Point out each Plasmodium parasite.
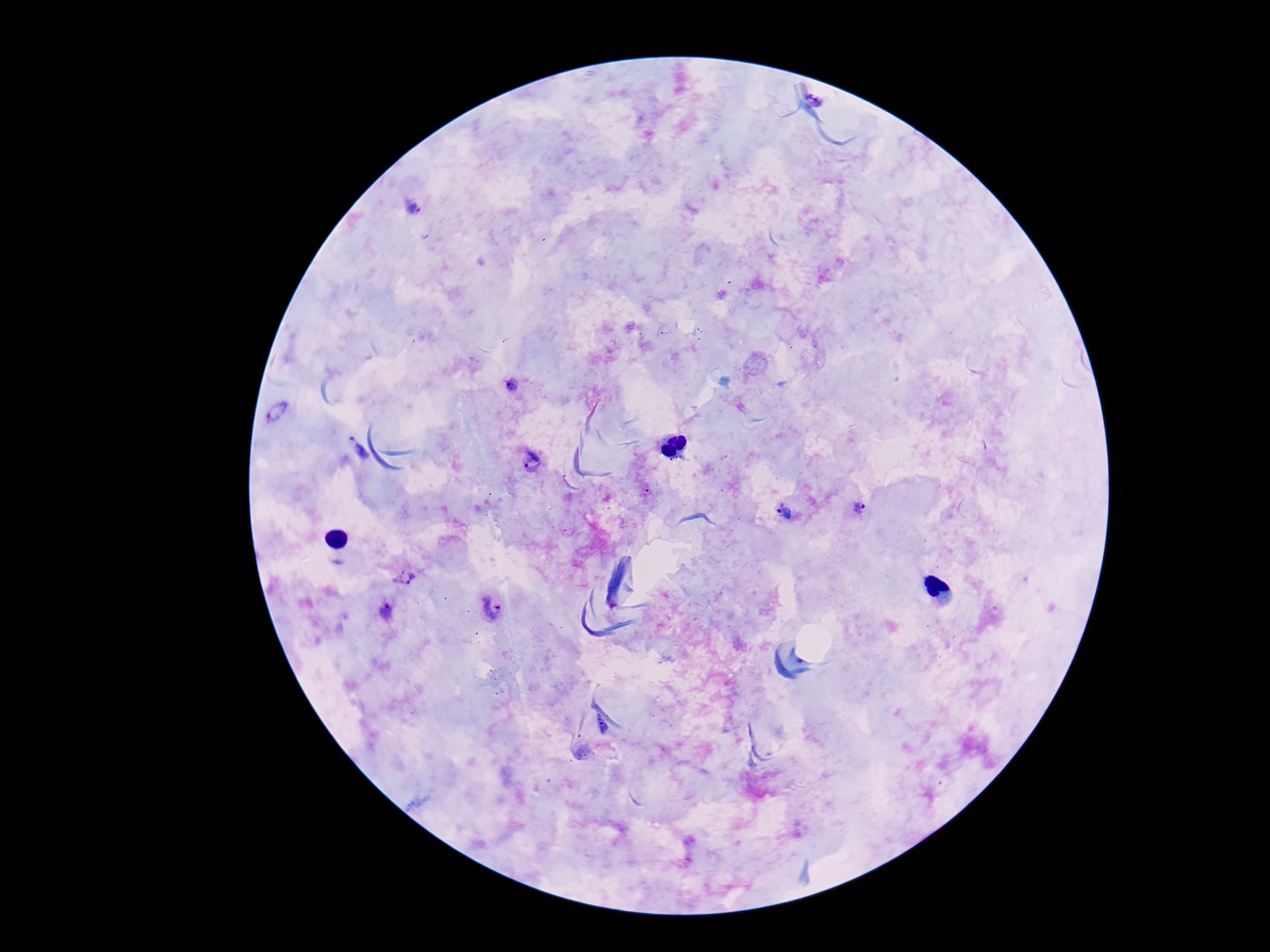
Approximate centers as (x, y) in pixels.
Plasmodium parasites: (413, 209), (512, 385), (531, 462), (858, 508), (783, 512), (492, 610), (388, 611).

Summary:
  - Field of view: single
  - Patient malaria status: infected
  - Capture: smartphone camera through the microscope eyepiece
  - Image size: 1270×952 pixels
  - Stain: Giemsa
  - Magnification: 100x
  - Preparation: thick blood film